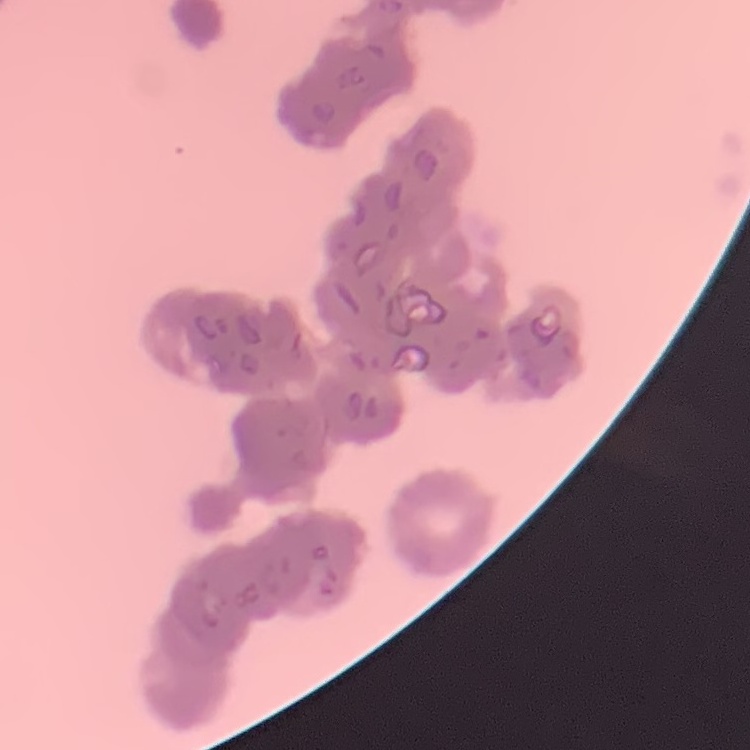
erythrocyte morphology = rouleaux formation
stain = Field's or Giemsa
preparation = thin blood film
image type = one tile cut from a larger photomicrograph